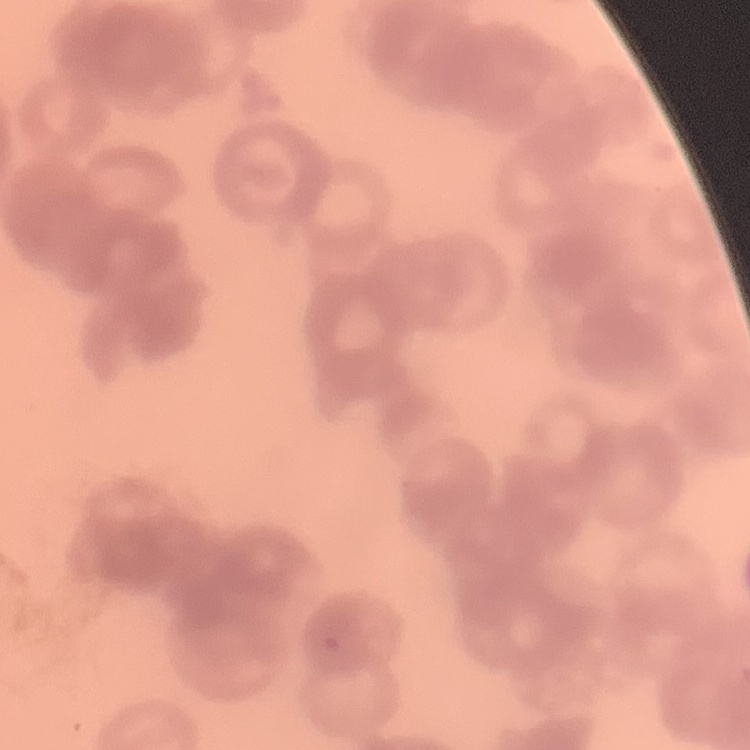

Summary:
  - Erythrocyte morphology: rouleaux formation
  - Image type: one tile cut from a larger photomicrograph
  - Preparation: thin blood smear
  - Stain: Field's or Giemsa